Report the malaria status of this cell.
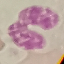
Uninfected.

Summary:
  - Capture: smartphone through the microscope eyepiece
  - Stain: Giemsa
  - Image type: automatically extracted cell patch, resized to 64 × 64 pixels
  - Preparation: thin smear